Describe the morphology of the erythrocytes.
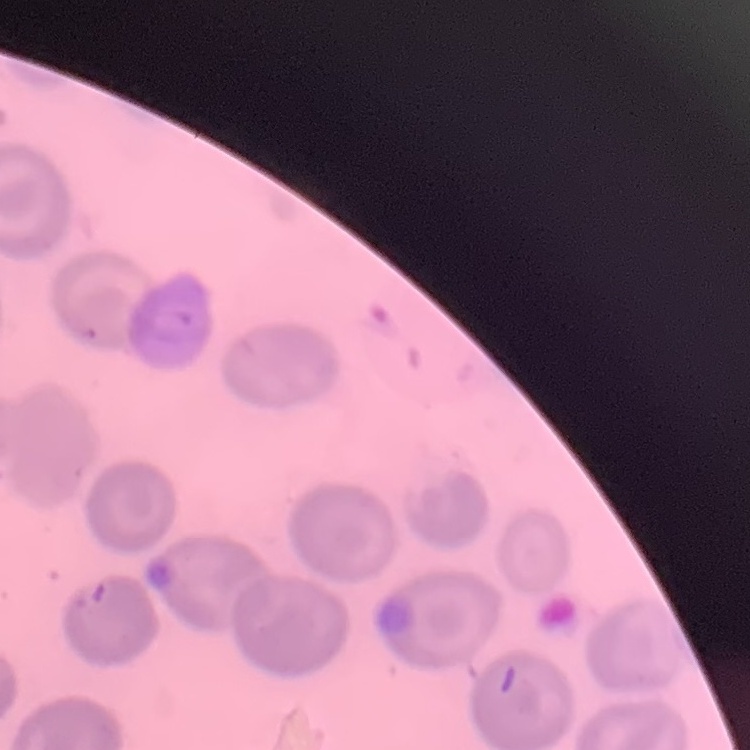
No rouleaux formation.

Field's or Giemsa stain. Thin blood smear. Square crop of a larger photomicrograph.